Describe the morphology of the erythrocytes.
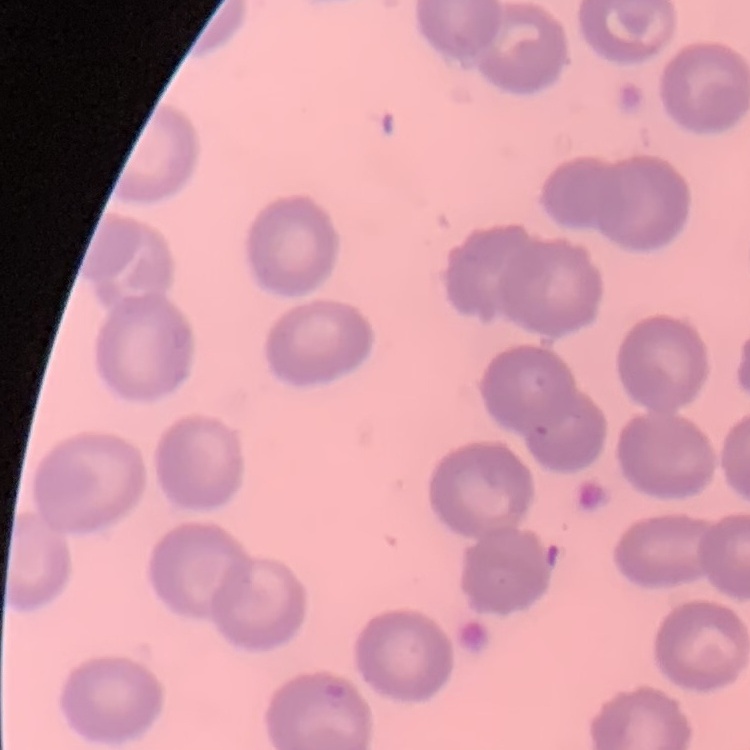
They show no rouleaux formation.

Stained with either Field's or Giemsa. Thin blood smear. Square crop of a larger photomicrograph.